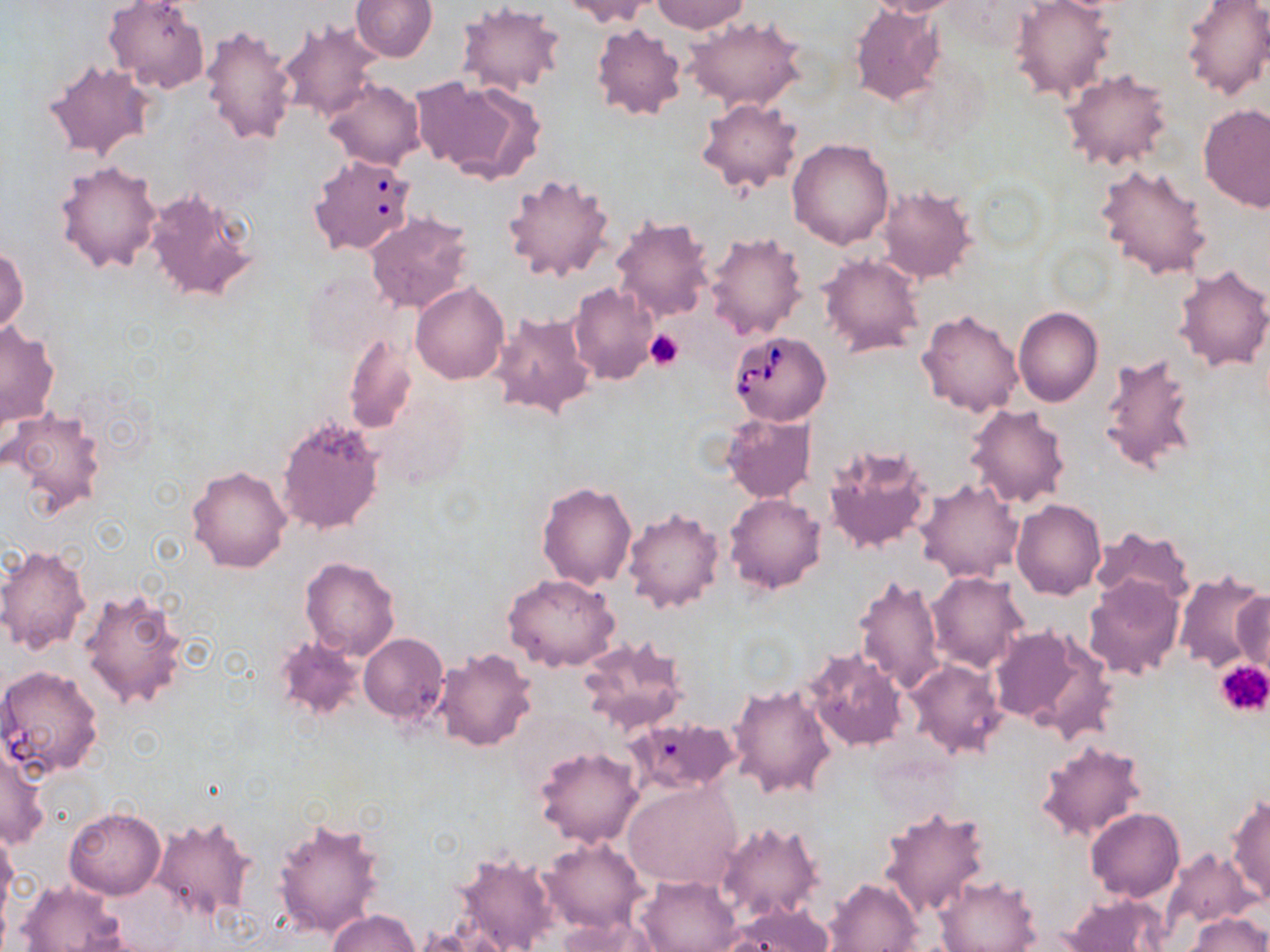

Summary:
  - Coordinate format: approximate bounding boxes as (x1, y1, x2, y2) in pixels
  - Babesia divergens-infected red blood cell locations: (312, 155, 413, 255), (729, 330, 831, 424), (1, 665, 104, 777)
  - Uninfected red blood cell locations: (352, 0, 438, 62), (558, 0, 661, 28), (649, 0, 751, 34), (863, 0, 971, 17), (1179, 0, 1270, 100), (103, 1, 211, 92), (1010, 1, 1118, 103), (848, 3, 948, 107), (456, 4, 567, 96), (684, 15, 809, 112), (276, 19, 382, 123), (591, 23, 688, 123), (199, 24, 298, 147), (43, 59, 155, 162), (1061, 69, 1174, 171), (411, 74, 543, 183), (323, 78, 426, 169), (696, 98, 803, 193), (1199, 104, 1269, 212), (788, 138, 895, 249), (54, 159, 162, 273), (1096, 161, 1211, 280), (502, 172, 615, 283), (877, 185, 976, 284), (144, 188, 260, 303), (364, 210, 476, 315), (611, 213, 715, 321), (704, 231, 808, 340), (0, 245, 28, 337), (817, 253, 924, 359), (1173, 263, 1270, 372), (410, 281, 510, 384), (567, 281, 659, 385), (1013, 307, 1104, 406), (916, 308, 1023, 418), (487, 310, 597, 420), (0, 321, 61, 429), (344, 333, 418, 435), (1098, 351, 1201, 479), (963, 402, 1072, 509), (3, 407, 108, 518), (721, 412, 816, 502), (276, 415, 386, 534), (824, 444, 934, 558), (186, 464, 292, 573), (915, 477, 1025, 583), (536, 482, 636, 590), (724, 493, 826, 594), (1010, 498, 1107, 599), (622, 507, 727, 616), (1091, 526, 1198, 610), (0, 544, 91, 653), (301, 556, 400, 660), (927, 571, 1030, 674), (1173, 571, 1270, 674), (503, 573, 621, 672), (852, 573, 945, 695), (1083, 574, 1186, 681), (78, 585, 192, 713), (1231, 585, 1270, 674), (989, 624, 1105, 733), (358, 633, 447, 726), (578, 634, 688, 735), (272, 636, 365, 721), (803, 647, 909, 751), (432, 648, 539, 753), (905, 658, 1010, 760), (727, 682, 838, 799), (614, 720, 744, 794), (1035, 739, 1149, 842), (0, 743, 50, 851), (534, 746, 645, 848), (623, 782, 741, 891), (1226, 794, 1270, 907), (878, 804, 991, 918), (65, 806, 165, 899), (1086, 807, 1184, 901), (151, 812, 257, 925), (272, 815, 387, 940), (714, 818, 825, 923), (0, 827, 18, 926), (539, 837, 648, 933), (449, 848, 559, 952), (1164, 849, 1258, 930), (934, 873, 1043, 952), (636, 874, 742, 952), (824, 877, 922, 952), (17, 880, 127, 951), (1060, 892, 1172, 952), (725, 901, 834, 951), (328, 909, 421, 952), (1187, 912, 1268, 952), (556, 917, 661, 952)
  - Platelet locations: (643, 329, 685, 374), (1215, 660, 1270, 717)
  - Slide-level diagnosis: Babesia divergens
  - Field of view: single
  - Preparation: thin blood film
  - Stain: May-Grünwald-Giemsa
  - Image size: 1270×952 pixels
  - Magnification: 1000x
  - Modality: optical microscopy